Identify the cell.
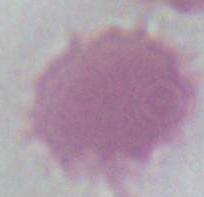
An erythrocyte.

{
  "modality": "micrograph",
  "magnification": "1000x"
}